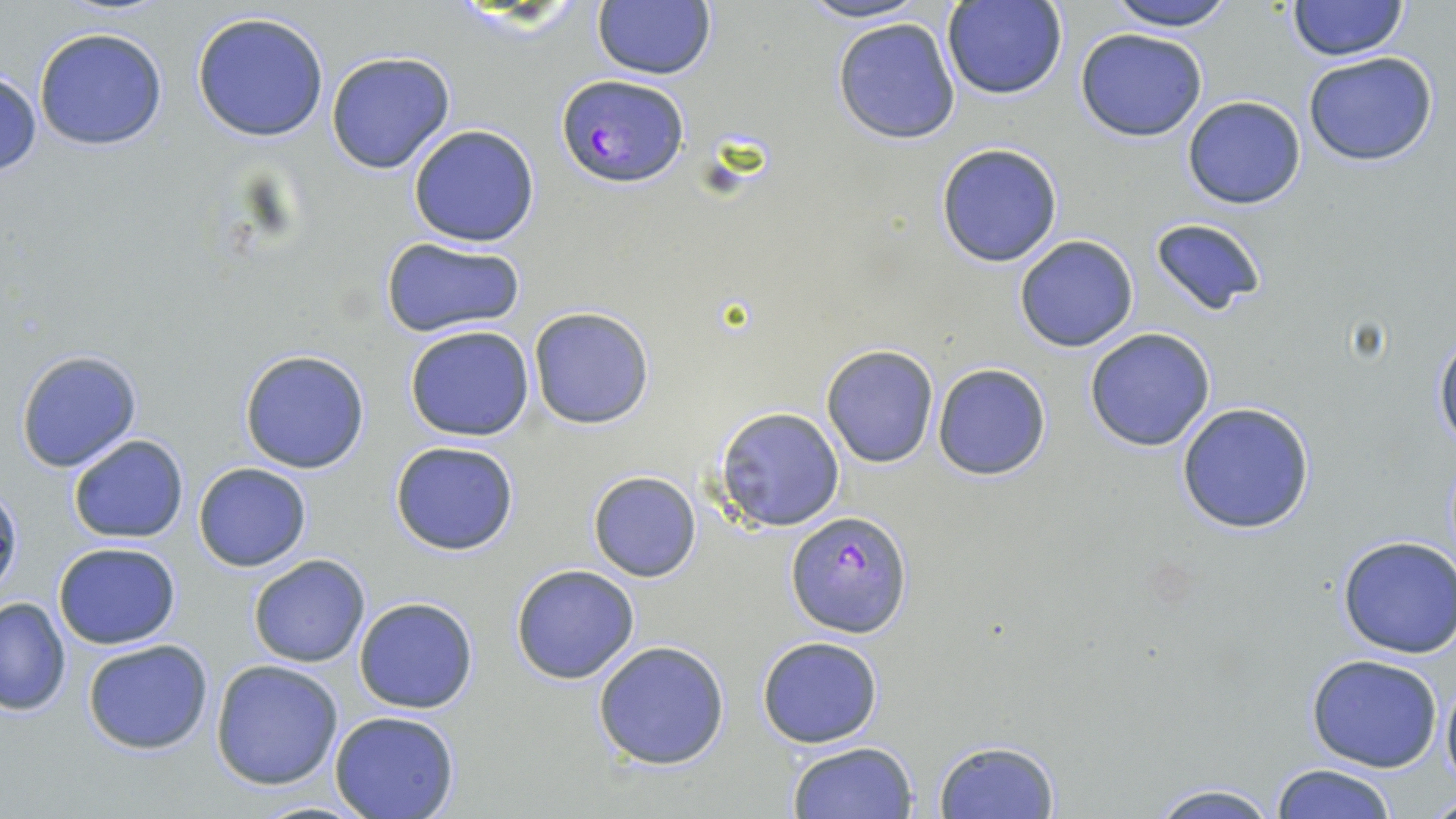

Approximate bounding boxes as [x1, y1, x2, y2] in pixels. Plasmodium falciparum-infected red blood cell locations: [556, 73, 687, 188], [786, 509, 914, 638]. Uninfected red blood cell locations: [793, 0, 932, 25], [1103, 0, 1241, 31], [1287, 0, 1407, 61], [593, 1, 715, 80], [942, 1, 1068, 100], [189, 10, 332, 142], [832, 18, 962, 144], [33, 26, 168, 151], [1076, 29, 1207, 142], [1302, 50, 1439, 167], [325, 51, 456, 175], [0, 70, 42, 179], [1183, 97, 1307, 209], [407, 124, 540, 248], [935, 142, 1064, 267], [1148, 216, 1268, 317], [1014, 235, 1140, 352], [381, 238, 525, 340], [528, 308, 654, 429], [404, 325, 536, 442], [1084, 327, 1217, 452], [1431, 328, 1456, 454], [822, 345, 940, 467], [15, 348, 143, 473], [238, 348, 370, 474], [931, 362, 1053, 481], [1173, 401, 1318, 536], [714, 406, 846, 533], [67, 435, 188, 544], [390, 439, 520, 556], [192, 462, 311, 571], [588, 470, 702, 582], [0, 482, 23, 603], [1336, 534, 1456, 659], [54, 542, 182, 649], [248, 554, 371, 668], [510, 563, 639, 684], [0, 596, 71, 715], [355, 598, 477, 714], [757, 636, 884, 749], [81, 638, 214, 755], [591, 640, 732, 771], [1306, 654, 1445, 773], [210, 659, 344, 790], [1439, 665, 1456, 794], [329, 711, 461, 819], [935, 739, 1060, 817], [787, 742, 918, 819], [1268, 762, 1400, 819], [1140, 780, 1283, 818], [1424, 789, 1456, 817]. Slide-level diagnosis: Plasmodium falciparum. Light microscopy. May-Grünwald-Giemsa-stained preparation. One field of a larger specimen. Thin blood film. Captured at 1000x magnification. Image is 1456×819 pixels.